Name the cell type shown.
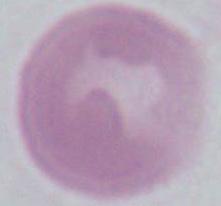

An erythrocyte.

Summary:
  - Magnification: 1000x
  - Modality: micrograph